Report the malaria status of this cell.
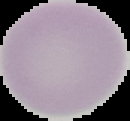

It is uninfected.

preparation = thin blood smear
image size = 130×121 pixels
image type = segmented cell region on a black background